Locate every blood parasite and identify its species.
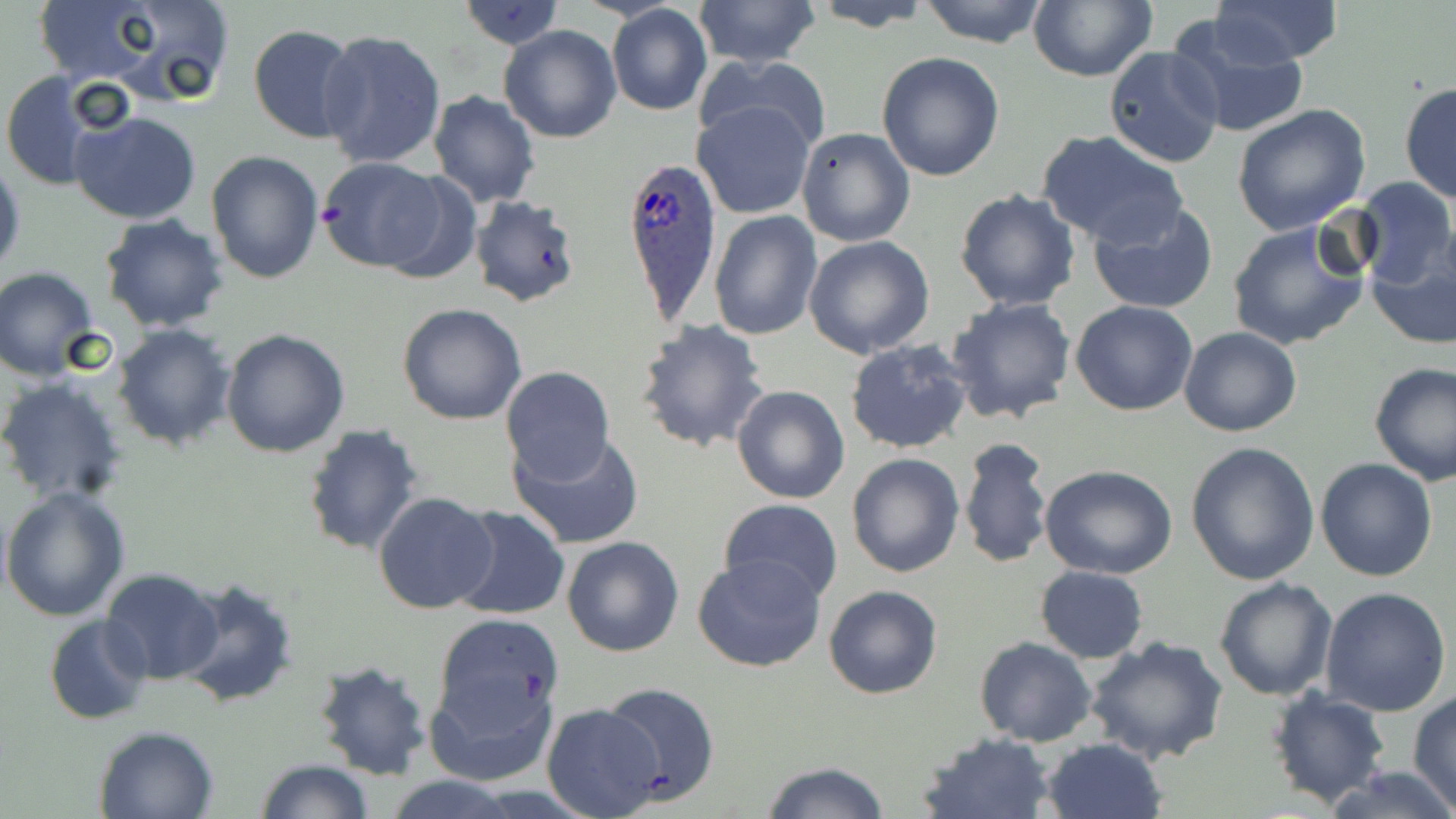

Approximate bounding boxes as (x1, y1, x2, y2) in pixels.
Plasmodium ovale-infected red blood cells: (619, 153, 720, 325).
No Plasmodium falciparum, Plasmodium malariae, Plasmodium vivax, Babesia divergens, or Trypanosoma brucei observed.

slide-level diagnosis = Plasmodium ovale
image size = 1456×819 pixels
modality = light microscopy
field of view = one of a larger specimen
stain = May-Grünwald-Giemsa
preparation = thin blood film
uninfected red blood cell locations = approximate bounding boxes as (x1, y1, x2, y2) in pixels: (26, 0, 178, 88), (88, 0, 237, 105), (691, 0, 821, 70), (918, 0, 1049, 46), (1028, 0, 1156, 83), (1210, 0, 1343, 65), (459, 1, 564, 50), (804, 1, 936, 31), (606, 5, 713, 117), (1167, 13, 1309, 142), (248, 24, 360, 143), (499, 24, 622, 143), (318, 28, 447, 170), (1103, 46, 1225, 170), (876, 52, 1005, 181), (696, 53, 834, 158), (0, 72, 106, 192), (1399, 81, 1456, 205), (428, 91, 541, 207), (693, 99, 817, 218), (1231, 103, 1371, 235), (71, 109, 202, 225), (795, 127, 916, 248), (1036, 130, 1188, 248), (206, 149, 324, 284), (0, 156, 25, 280), (315, 157, 453, 273), (1351, 176, 1455, 287), (954, 188, 1081, 311), (468, 194, 584, 309), (1086, 200, 1219, 315), (709, 210, 823, 341), (99, 214, 230, 332), (1226, 218, 1372, 351), (803, 235, 935, 359), (1366, 246, 1456, 350), (1, 268, 101, 380), (946, 296, 1077, 424), (1071, 301, 1198, 417), (396, 302, 528, 426), (635, 318, 770, 454), (112, 323, 238, 450), (1178, 327, 1303, 437), (221, 329, 350, 459), (843, 338, 972, 455), (1368, 360, 1456, 485), (498, 365, 616, 486), (0, 376, 129, 506), (731, 384, 850, 505), (302, 424, 423, 558), (508, 431, 646, 550), (958, 437, 1053, 570), (1185, 441, 1320, 584), (846, 452, 964, 577), (1315, 458, 1438, 582), (1039, 463, 1178, 579), (1, 486, 130, 621), (372, 490, 497, 615), (719, 498, 843, 603), (448, 505, 570, 621), (562, 535, 686, 658), (692, 554, 826, 673), (1035, 566, 1148, 663), (100, 568, 226, 685), (174, 575, 299, 709), (1213, 577, 1338, 701), (823, 585, 943, 699), (1320, 587, 1452, 717), (43, 614, 152, 726), (432, 614, 564, 746), (1082, 635, 1229, 765), (975, 637, 1097, 747), (311, 659, 434, 781), (423, 665, 559, 788), (600, 681, 720, 804), (1266, 687, 1392, 807), (1408, 692, 1456, 810), (540, 703, 664, 817), (93, 724, 221, 818), (918, 732, 1056, 818), (1040, 737, 1166, 819), (253, 759, 374, 818), (758, 761, 892, 819), (1325, 764, 1456, 819), (381, 774, 523, 818)
magnification = 1000x